Describe the morphology of the erythrocytes.
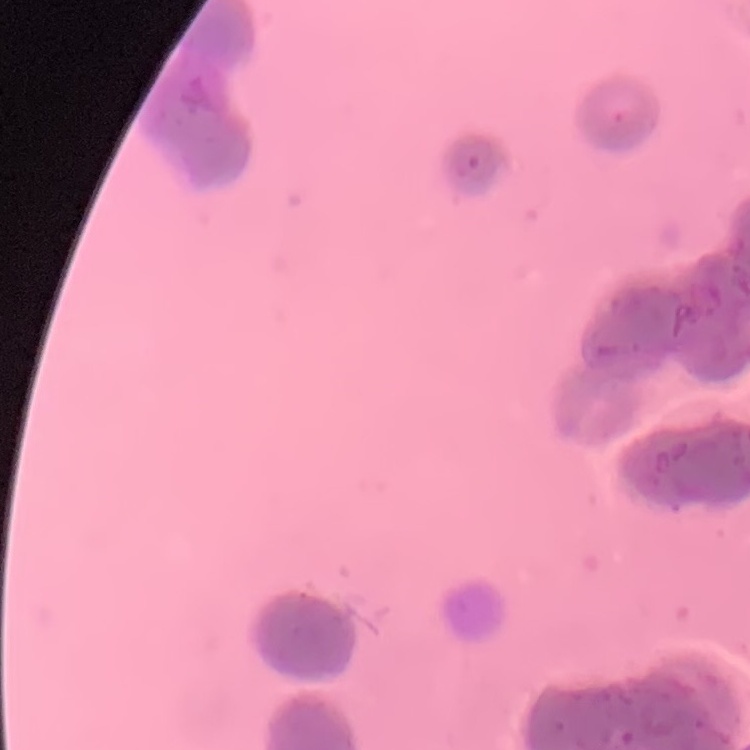
Rouleaux formation.

Summary:
  - Preparation: thin peripheral smear
  - Image type: square crop of a larger photomicrograph
  - Stain: Field's or Giemsa